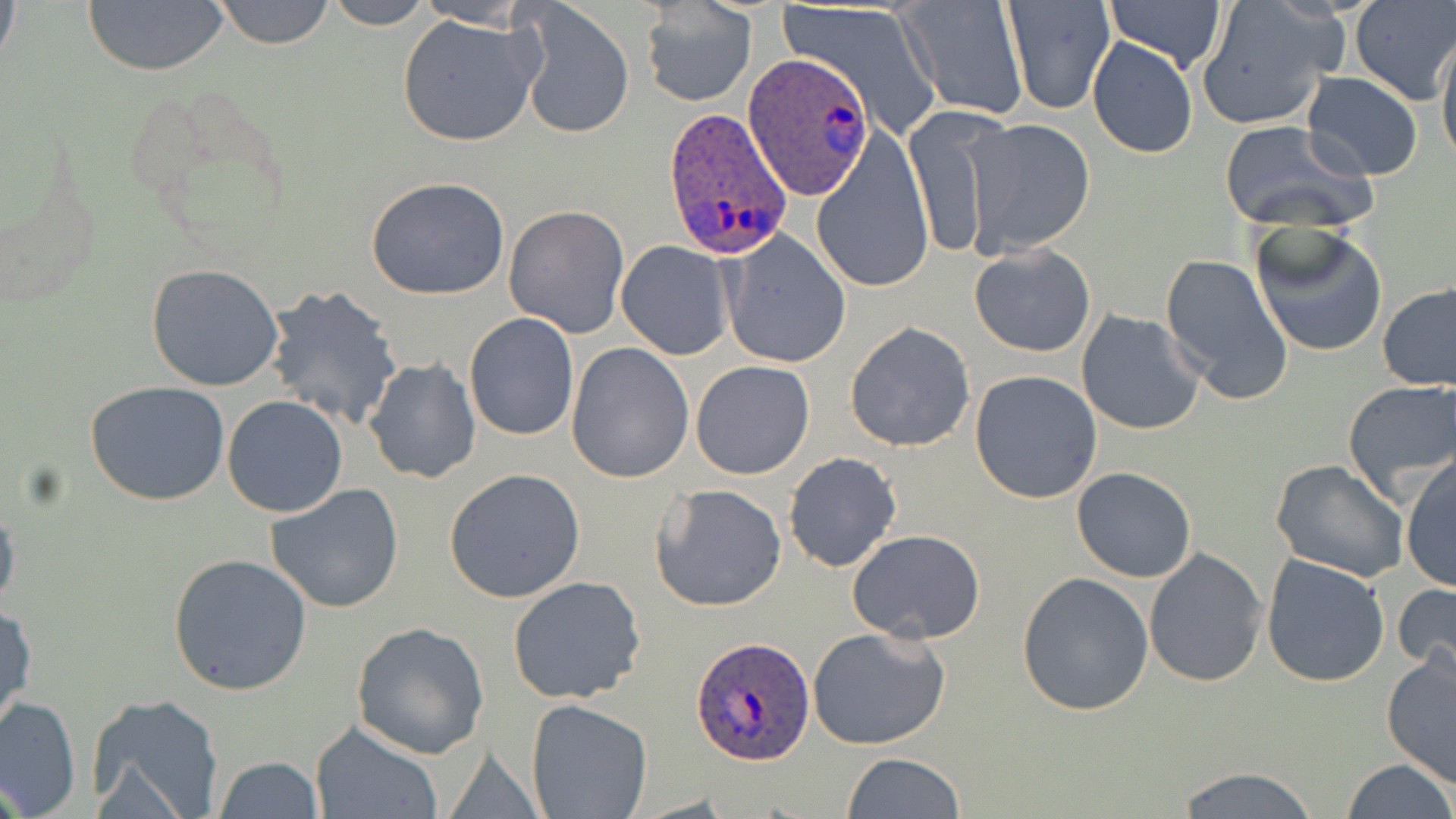

Summary:
  - Coordinate format: approximate bounding boxes as (x1, y1, x2, y2) in pixels
  - Uninfected red blood cell locations: (210, 0, 335, 48), (319, 0, 436, 28), (1103, 0, 1228, 75), (1352, 0, 1456, 105), (84, 1, 228, 76), (514, 1, 636, 140), (641, 2, 757, 108), (779, 2, 941, 130), (896, 2, 1029, 123), (1003, 2, 1112, 116), (1197, 2, 1347, 131), (397, 13, 540, 147), (1437, 32, 1456, 169), (1088, 37, 1198, 160), (1302, 72, 1424, 181), (905, 108, 1007, 262), (963, 118, 1096, 256), (1219, 122, 1376, 234), (810, 128, 936, 294), (365, 176, 512, 301), (504, 204, 631, 337), (1248, 220, 1388, 358), (722, 233, 850, 367), (615, 241, 734, 360), (969, 243, 1095, 357), (1160, 254, 1294, 405), (146, 263, 286, 393), (1378, 284, 1456, 392), (265, 287, 405, 431), (1076, 310, 1204, 435), (463, 312, 579, 442), (845, 319, 975, 452), (566, 342, 694, 484), (364, 358, 480, 484), (690, 361, 816, 480), (969, 370, 1102, 504), (85, 380, 230, 506), (1342, 380, 1456, 505), (221, 395, 348, 518), (784, 451, 902, 573), (1400, 456, 1456, 594), (1270, 459, 1409, 584), (1071, 466, 1198, 583), (443, 468, 587, 603), (264, 482, 406, 614), (649, 483, 788, 612), (0, 499, 21, 620), (847, 528, 986, 644), (1145, 548, 1268, 688), (168, 552, 313, 696), (1260, 553, 1390, 688), (1016, 571, 1154, 715), (507, 575, 646, 704), (1394, 579, 1456, 684), (1, 601, 36, 735), (353, 622, 491, 758), (806, 625, 954, 752), (1382, 648, 1456, 787), (86, 692, 224, 819), (0, 696, 81, 818), (526, 700, 653, 819), (310, 721, 441, 819), (841, 752, 965, 818), (211, 755, 324, 819), (1341, 759, 1454, 819), (1174, 765, 1322, 819)
  - Plasmodium ovale-infected red blood cell locations: (744, 53, 875, 200), (660, 106, 793, 260), (689, 634, 815, 764)
  - Slide-level diagnosis: Plasmodium ovale
  - Magnification: 1000x
  - Preparation: thin blood smear
  - Stain: May-Grünwald-Giemsa
  - Field of view: single
  - Image size: 1456×819 pixels
  - Modality: light microscopy